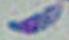

identification = Toxoplasma gondii
magnification = 1000x
modality = photomicrograph